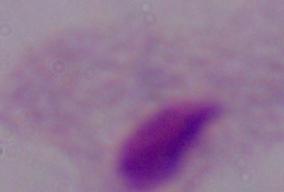

Summary:
  - Magnification: 1000x
  - Modality: micrograph
  - Identification: trichomonad